Report the malaria status of this cell.
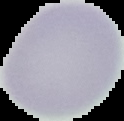
Uninfected.

preparation: thin blood film
image_size: 124×121 pixels
image_type: segmented cell region on a black background